State the preparation type.
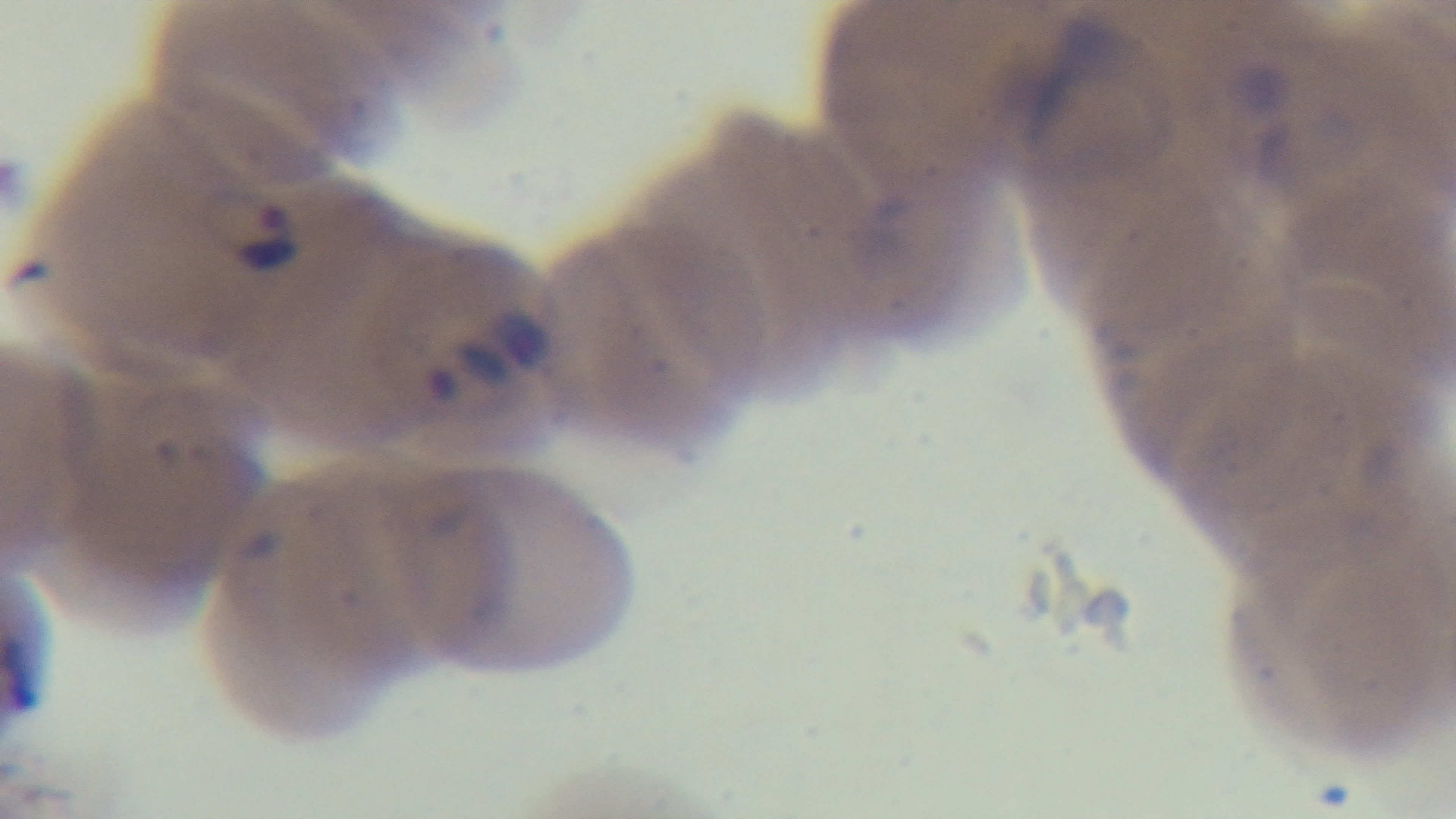

It is a thin blood film.

Summary:
  - Malaria status: positive
  - Field of view: single
  - Objective: 100x oil immersion
  - Stain: Giemsa
  - Capture: mounted 4K digital camera
  - Modality: light microscopy